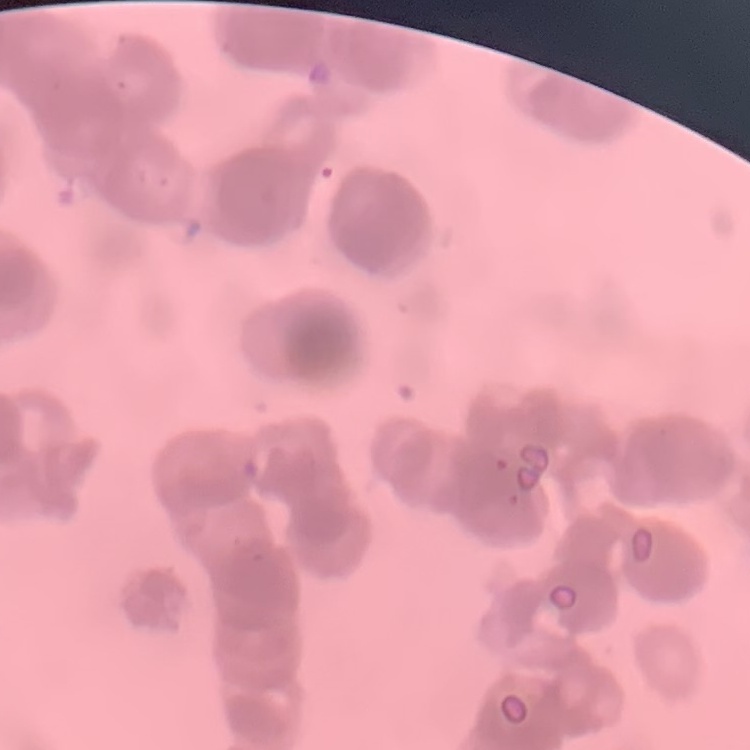
Summary:
  - Erythrocyte morphology: rouleaux formation
  - Stain: Field's or Giemsa
  - Preparation: thin peripheral smear
  - Image type: one tile cut from a larger photomicrograph